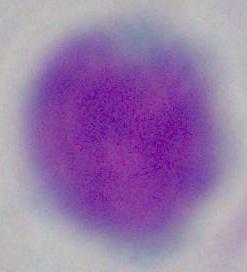
A white blood cell is shown. 1000x magnification. Micrograph.